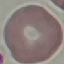

Summary:
  - Result: no malaria parasites seen
  - Capture: smartphone camera at the microscope eyepiece
  - Stain: Giemsa
  - Preparation: thin blood smear
  - Image type: cell patch, automatically extracted from a larger field of view and resized to 64 × 64 pixels